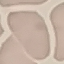
Summary:
  - Malaria status: uninfected
  - Preparation: thin blood film
  - Stain: Giemsa
  - Image type: cell patch, automatically extracted from a larger field of view and resized to 64 × 64 pixels
  - Capture: smartphone camera at the microscope eyepiece